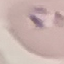 Result: malaria parasites detected. Automatically extracted cell patch, resized to 64 × 64 pixels. Acquired by smartphone through the microscope eyepiece. Giemsa-stained preparation. Thin blood smear.